Identify the parasite.
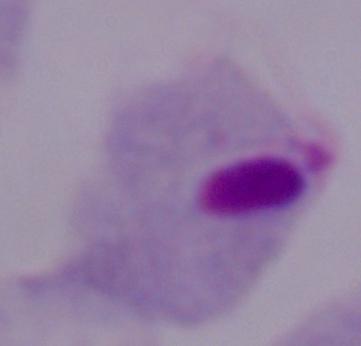
This is a trichomonad.

Micrograph. 1000x magnification.